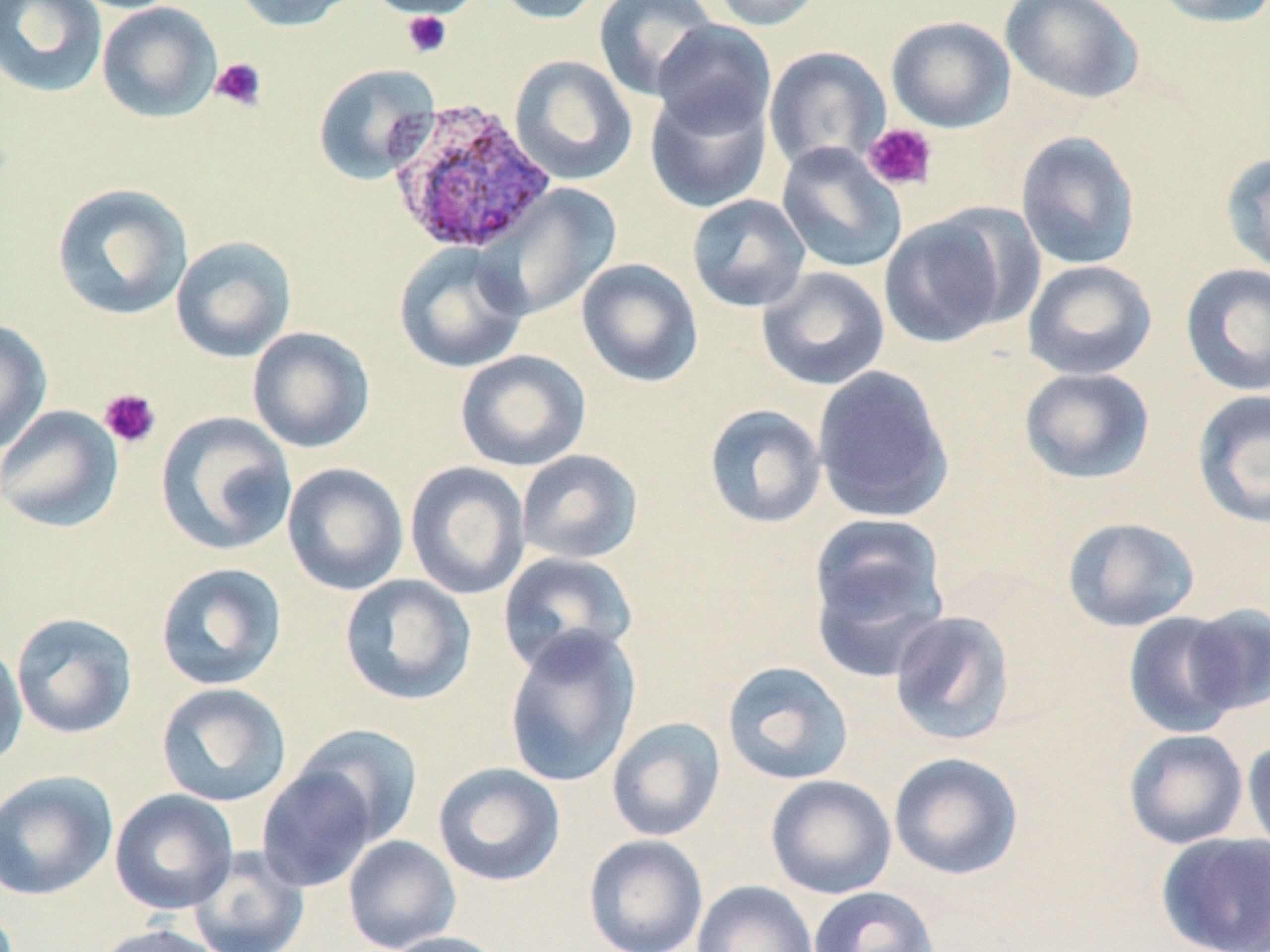
Summary:
  - Coordinate format: approximate bounding boxes as (x1, y1, x2, y2) in pixels
  - Uninfected red blood cell locations: (0, 0, 109, 99), (228, 0, 362, 32), (362, 0, 487, 19), (491, 0, 605, 24), (592, 0, 719, 101), (707, 0, 826, 31), (999, 0, 1145, 105), (1150, 0, 1270, 28), (96, 2, 222, 123), (886, 15, 1016, 133), (651, 19, 777, 139), (764, 46, 892, 173), (508, 54, 638, 186), (313, 63, 441, 185), (645, 86, 772, 213), (1015, 130, 1141, 270), (776, 142, 906, 274), (1220, 151, 1270, 277), (51, 182, 194, 321), (480, 183, 624, 320), (686, 194, 811, 313), (879, 212, 1014, 349), (170, 235, 297, 363), (393, 242, 530, 374), (576, 258, 703, 388), (1022, 259, 1156, 380), (1180, 263, 1270, 396), (756, 266, 890, 391), (0, 318, 52, 455), (246, 327, 376, 454), (455, 350, 592, 472), (812, 365, 955, 524), (1019, 367, 1155, 485), (1191, 388, 1270, 530), (703, 404, 826, 529), (0, 405, 123, 533), (156, 411, 297, 556), (516, 449, 643, 565), (405, 461, 531, 600), (281, 462, 409, 596), (808, 515, 950, 652), (1062, 516, 1201, 632), (497, 550, 639, 675), (155, 562, 288, 691), (339, 574, 477, 706), (1184, 603, 1270, 716), (889, 610, 1016, 746), (1123, 611, 1244, 738), (11, 612, 138, 740), (503, 626, 640, 789), (0, 636, 28, 773), (721, 661, 855, 785), (156, 683, 292, 807), (606, 716, 725, 842), (293, 723, 424, 845), (1123, 728, 1249, 849), (1242, 735, 1270, 859), (888, 752, 1024, 881), (432, 762, 566, 887), (257, 766, 378, 892), (0, 770, 118, 901), (765, 775, 897, 899), (109, 789, 239, 915), (1155, 832, 1270, 952), (342, 834, 461, 952), (583, 834, 709, 952), (188, 846, 310, 952), (692, 881, 819, 952), (808, 885, 939, 952), (95, 924, 225, 952), (381, 931, 508, 952)
  - Platelet locations: (401, 11, 452, 58), (210, 58, 268, 112), (862, 122, 939, 192), (99, 388, 161, 448)
  - Plasmodium ovale-infected red blood cell locations: (386, 98, 558, 256)
  - Slide-level diagnosis: Plasmodium ovale
  - Stain: May-Grünwald-Giemsa
  - Image size: 1270×952 pixels
  - Magnification: 1000x
  - Modality: optical microscopy
  - Preparation: thin blood smear
  - Field of view: single